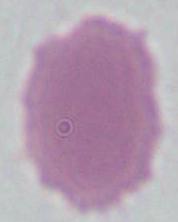

identification = red blood cell
magnification = 1000x
modality = photomicrograph